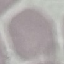 Malaria status: uninfected. Giemsa stain. Thin smear of blood. Cell patch, automatically extracted from a larger field of view and resized to 64 × 64 pixels. Photographed with a smartphone camera at the microscope eyepiece.